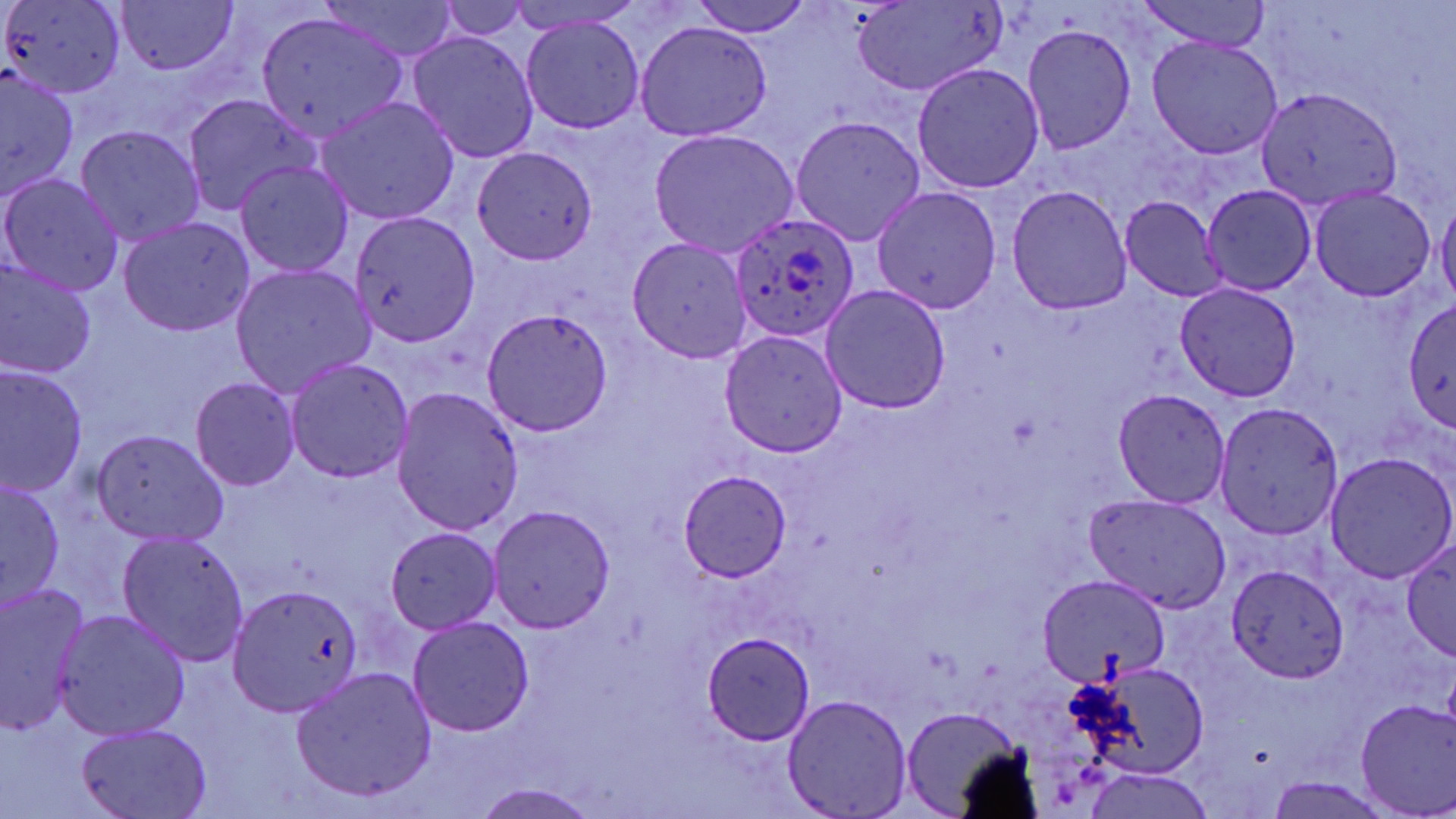

Summary:
  - Coordinate format: approximate bounding boxes as named x1/y1/x2/y2 corners in pixels
  - Uninfected red blood cell locations: (x1=113, y1=0, x2=239, y2=77), (x1=433, y1=0, x2=541, y2=43), (x1=687, y1=0, x2=817, y2=37), (x1=848, y1=0, x2=1009, y2=98), (x1=1132, y1=0, x2=1279, y2=48), (x1=1, y1=1, x2=126, y2=102), (x1=323, y1=1, x2=459, y2=61), (x1=257, y1=9, x2=417, y2=142), (x1=520, y1=15, x2=646, y2=135), (x1=634, y1=21, x2=772, y2=142), (x1=1019, y1=22, x2=1138, y2=157), (x1=406, y1=29, x2=541, y2=165), (x1=1145, y1=33, x2=1282, y2=161), (x1=910, y1=61, x2=1045, y2=194), (x1=0, y1=68, x2=81, y2=197), (x1=1254, y1=85, x2=1399, y2=209), (x1=179, y1=92, x2=319, y2=216), (x1=314, y1=95, x2=460, y2=227), (x1=789, y1=114, x2=927, y2=246), (x1=70, y1=123, x2=206, y2=247), (x1=647, y1=126, x2=801, y2=258), (x1=470, y1=145, x2=595, y2=264), (x1=233, y1=158, x2=355, y2=280), (x1=0, y1=169, x2=124, y2=297), (x1=870, y1=184, x2=1002, y2=317), (x1=1004, y1=184, x2=1134, y2=317), (x1=1201, y1=184, x2=1317, y2=296), (x1=1305, y1=184, x2=1437, y2=303), (x1=1435, y1=194, x2=1456, y2=308), (x1=1120, y1=195, x2=1228, y2=304), (x1=346, y1=209, x2=482, y2=347), (x1=115, y1=215, x2=257, y2=337), (x1=624, y1=236, x2=751, y2=362), (x1=0, y1=256, x2=98, y2=381), (x1=227, y1=262, x2=378, y2=394), (x1=1174, y1=280, x2=1304, y2=405), (x1=819, y1=283, x2=952, y2=415), (x1=1404, y1=298, x2=1456, y2=435), (x1=480, y1=309, x2=615, y2=438), (x1=717, y1=327, x2=847, y2=459), (x1=282, y1=355, x2=414, y2=485), (x1=0, y1=361, x2=90, y2=500), (x1=187, y1=376, x2=301, y2=491), (x1=389, y1=385, x2=522, y2=538), (x1=1112, y1=386, x2=1235, y2=508), (x1=1215, y1=402, x2=1346, y2=543), (x1=88, y1=426, x2=231, y2=549), (x1=1323, y1=451, x2=1456, y2=583), (x1=670, y1=468, x2=796, y2=585), (x1=0, y1=474, x2=68, y2=613), (x1=1081, y1=491, x2=1232, y2=612), (x1=488, y1=504, x2=616, y2=634), (x1=386, y1=524, x2=505, y2=637), (x1=116, y1=528, x2=252, y2=667), (x1=1399, y1=539, x2=1456, y2=663), (x1=1225, y1=564, x2=1351, y2=684), (x1=1036, y1=575, x2=1170, y2=686), (x1=0, y1=578, x2=90, y2=736), (x1=226, y1=584, x2=367, y2=720), (x1=53, y1=608, x2=189, y2=743), (x1=405, y1=614, x2=537, y2=736), (x1=702, y1=632, x2=818, y2=745), (x1=1078, y1=657, x2=1213, y2=784), (x1=292, y1=666, x2=440, y2=803), (x1=780, y1=694, x2=913, y2=819), (x1=1354, y1=697, x2=1456, y2=818), (x1=899, y1=704, x2=1036, y2=816), (x1=73, y1=722, x2=214, y2=819), (x1=1086, y1=764, x2=1212, y2=817), (x1=469, y1=783, x2=600, y2=819)
  - Plasmodium ovale-infected red blood cell locations: (x1=725, y1=209, x2=861, y2=346)
  - Slide-level diagnosis: Plasmodium ovale
  - Modality: light microscopy
  - Stain: May-Grünwald-Giemsa
  - Field of view: single
  - Magnification: 1000x
  - Preparation: thin blood smear
  - Image size: 1456×819 pixels